Classify this cell by malaria status.
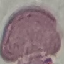
Uninfected.

Summary:
  - Stain: Giemsa
  - Image type: cell patch, automatically extracted from a larger field of view and resized to 64 × 64 pixels
  - Capture: smartphone through the microscope eyepiece
  - Preparation: thin smear